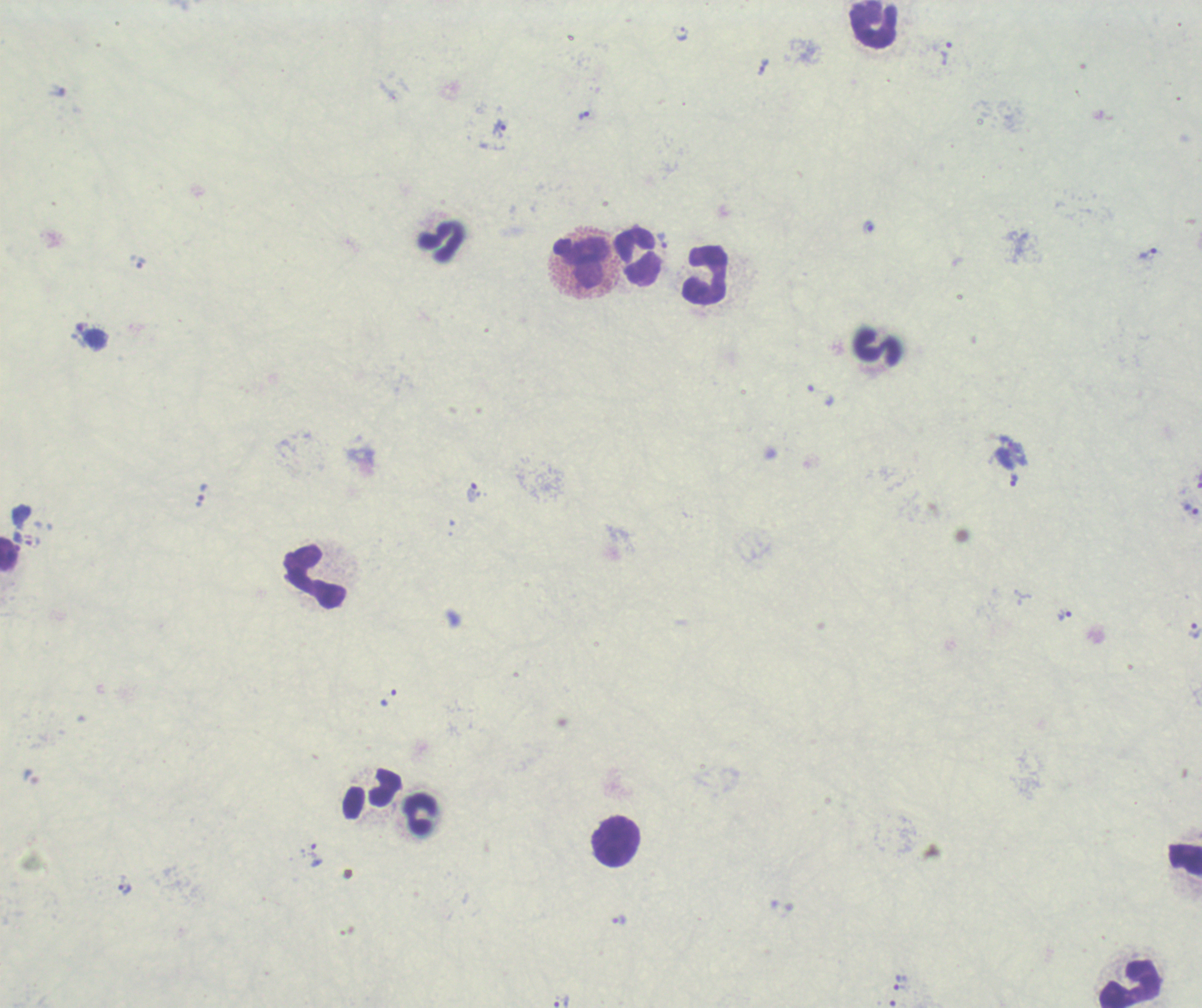

magnification: 100x
background_quality: poor
leukocyte_locations: 'approximate centers as [x, y] in pixels: [874, 25], [440, 241], [637, 256], [584, 262], [705, 275], [878, 347], [9, 555], [315, 575], [372, 793], [421, 814], [616, 841], [1185, 856], [1130, 983]'
preparation: thick blood film
context: previously used in a real diagnosis
field_of_view: single
trophozoite_locations: 'approximate centers as [x, y] in pixels: [682, 34], [946, 53], [763, 66], [583, 115], [500, 129], [868, 227], [662, 240], [1148, 253], [141, 263], [1013, 480], [472, 493], [201, 494], [1191, 509], [1064, 615], [1194, 631], [388, 698], [316, 855], [124, 890], [618, 920], [900, 983], [561, 1001]'
result: positive for Plasmodium parasites
image_size: 1202×1008 pixels
stain: Romanowsky